Identify the parasite.
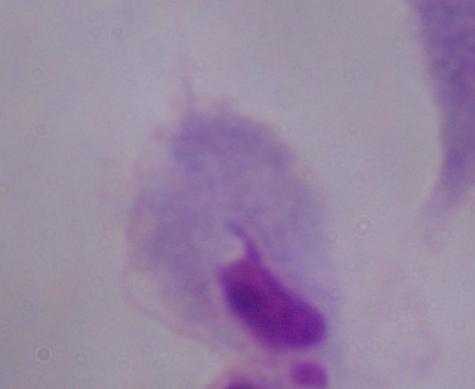
This is a trichomonad.

Photomicrograph. 1000x magnification.